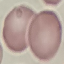 Result: no malaria parasites seen. Automatically extracted cell patch, resized to 64 × 64 pixels. Acquired by smartphone through the microscope eyepiece. Giemsa-stained preparation. Thin smear of blood.